Locate every Plasmodium parasite.
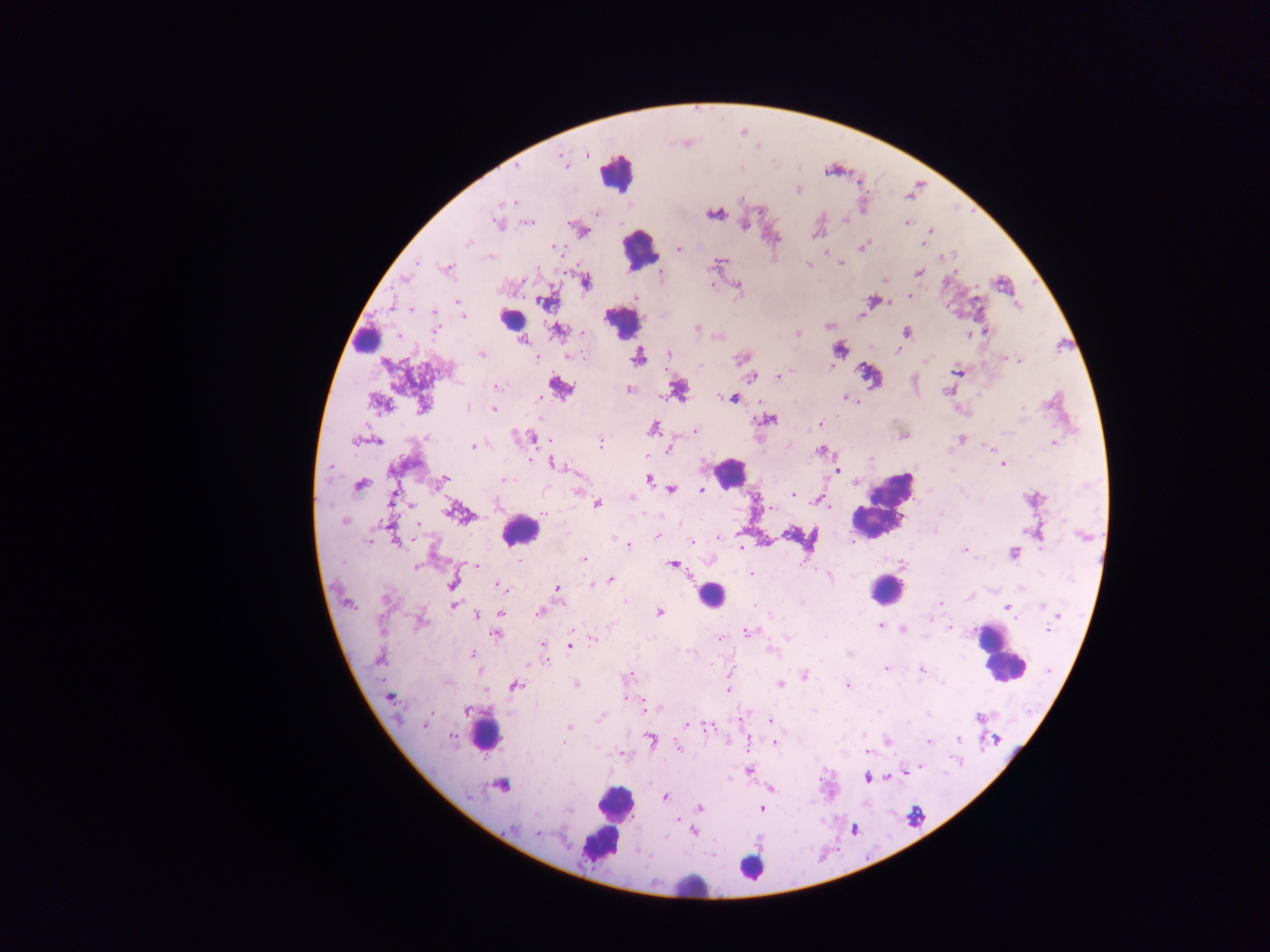
Approximate centers as {x, y} in pixels.
Plasmodium parasites: {587, 153}, {563, 160}, {516, 165}, {798, 190}, {512, 203}, {714, 213}, {596, 214}, {844, 219}, {496, 222}, {529, 222}, {907, 223}, {745, 224}, {930, 231}, {584, 232}, {816, 235}, {469, 242}, {922, 244}, {863, 246}, {554, 247}, {679, 248}, {490, 256}, {417, 262}, {719, 262}, {841, 262}, {807, 265}, {448, 268}, {956, 270}, {918, 272}, {660, 274}, {404, 279}, {586, 281}, {711, 284}, {737, 287}, {909, 296}, {635, 298}, {871, 300}, {546, 302}, {458, 303}, {1017, 306}, {412, 309}, {433, 312}, {861, 315}, {463, 316}, {829, 325}, {697, 328}, {436, 330}, {558, 331}, {583, 332}, {906, 332}, {986, 332}, {797, 333}, {526, 341}, {839, 349}, {898, 350}, {481, 354}, {669, 354}, {571, 355}, {638, 357}, {1005, 357}, {537, 358}, {743, 358}, {1019, 360}, {926, 361}, {700, 365}, {830, 366}, {956, 372}, {778, 376}, {751, 377}, {498, 386}, {560, 387}, {629, 389}, {947, 391}, {679, 392}, {539, 398}, {732, 398}, {846, 398}, {378, 404}, {423, 406}, {468, 407}, {493, 409}, {768, 419}, {819, 424}, {652, 429}, {695, 431}, {427, 436}, {534, 438}, {962, 439}, {354, 441}, {377, 441}, {601, 443}, {1053, 443}, {473, 446}, {991, 449}, {668, 450}, {821, 451}, {555, 465}, {1003, 465}, {330, 468}, {836, 469}, {443, 479}, {649, 479}, {505, 481}, {360, 484}, {672, 489}, {702, 489}, {578, 492}, {793, 494}, {631, 498}, {392, 500}, {597, 503}, {497, 504}, {823, 504}, {771, 508}, {451, 511}, {941, 512}, {544, 514}, {344, 521}, {656, 537}, {719, 537}, {369, 541}, {397, 541}, {692, 542}, {628, 545}, {741, 546}, {964, 549}, {1013, 554}, {584, 559}, {517, 560}, {672, 565}, {902, 565}, {476, 566}, {417, 568}, {750, 574}, {830, 576}, {610, 580}, {452, 584}, {592, 585}, {500, 586}, {557, 588}, {624, 602}, {941, 603}, {453, 605}, {1006, 606}, {1042, 607}, {540, 612}, {659, 612}, {501, 613}, {476, 615}, {1059, 616}, {420, 622}, {879, 626}, {903, 629}, {950, 629}, {1047, 630}, {748, 632}, {496, 634}, {720, 637}, {593, 639}, {542, 645}, {570, 645}, {772, 650}, {471, 654}, {379, 659}, {546, 661}, {886, 668}, {922, 669}, {628, 675}, {804, 675}, {575, 683}, {780, 684}, {848, 685}, {515, 686}, {728, 689}, {390, 698}, {625, 698}, {648, 708}, {467, 711}, {979, 717}, {600, 718}, {770, 720}, {425, 724}, {687, 724}, {707, 726}, {566, 727}, {452, 738}, {651, 740}, {959, 740}, {995, 740}, {887, 741}, {564, 742}, {929, 742}, {775, 743}, {679, 748}, {867, 751}, {622, 754}, {920, 768}, {749, 770}, {868, 779}, {501, 785}, {771, 789}, {664, 797}, {700, 808}, {762, 808}, {569, 811}, {676, 820}, {512, 828}, {684, 829}, {693, 832}, {538, 834}.

{
  "country": "Ghana",
  "image_size": "1270×952 pixels",
  "field_of_view": "single",
  "leukocyte_locations": "approximate centers as {x, y} in pixels: {617, 172}, {639, 250}, {511, 319}, {621, 324}, {369, 341}, {729, 472}, {882, 505}, {519, 531}, {886, 589}, {710, 595}, {998, 656}, {486, 732}, {614, 804}, {608, 826}, {751, 868}, {688, 884}",
  "capture": "mobile-phone photograph through a microscope",
  "preparation": "thick blood film"
}